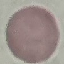

result = no malaria parasites seen
stain = Giemsa
image type = cell patch, automatically extracted from a larger field of view and resized to 64 × 64 pixels
preparation = thin blood film
capture = smartphone camera at the microscope eyepiece